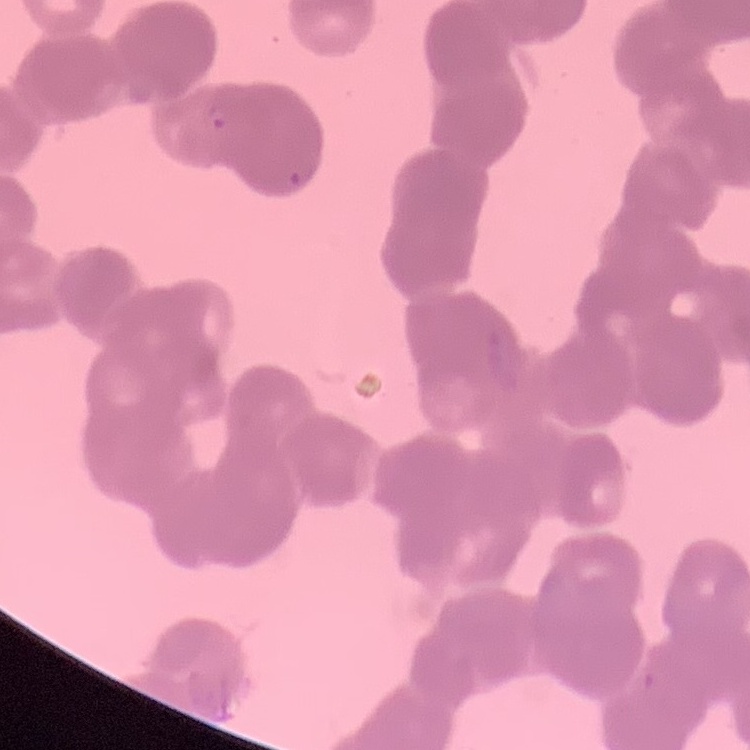

Summary:
  - Red blood cell morphology: rouleaux formation
  - Stain: Field's or Giemsa
  - Preparation: thin peripheral smear
  - Image type: square crop of a larger photomicrograph